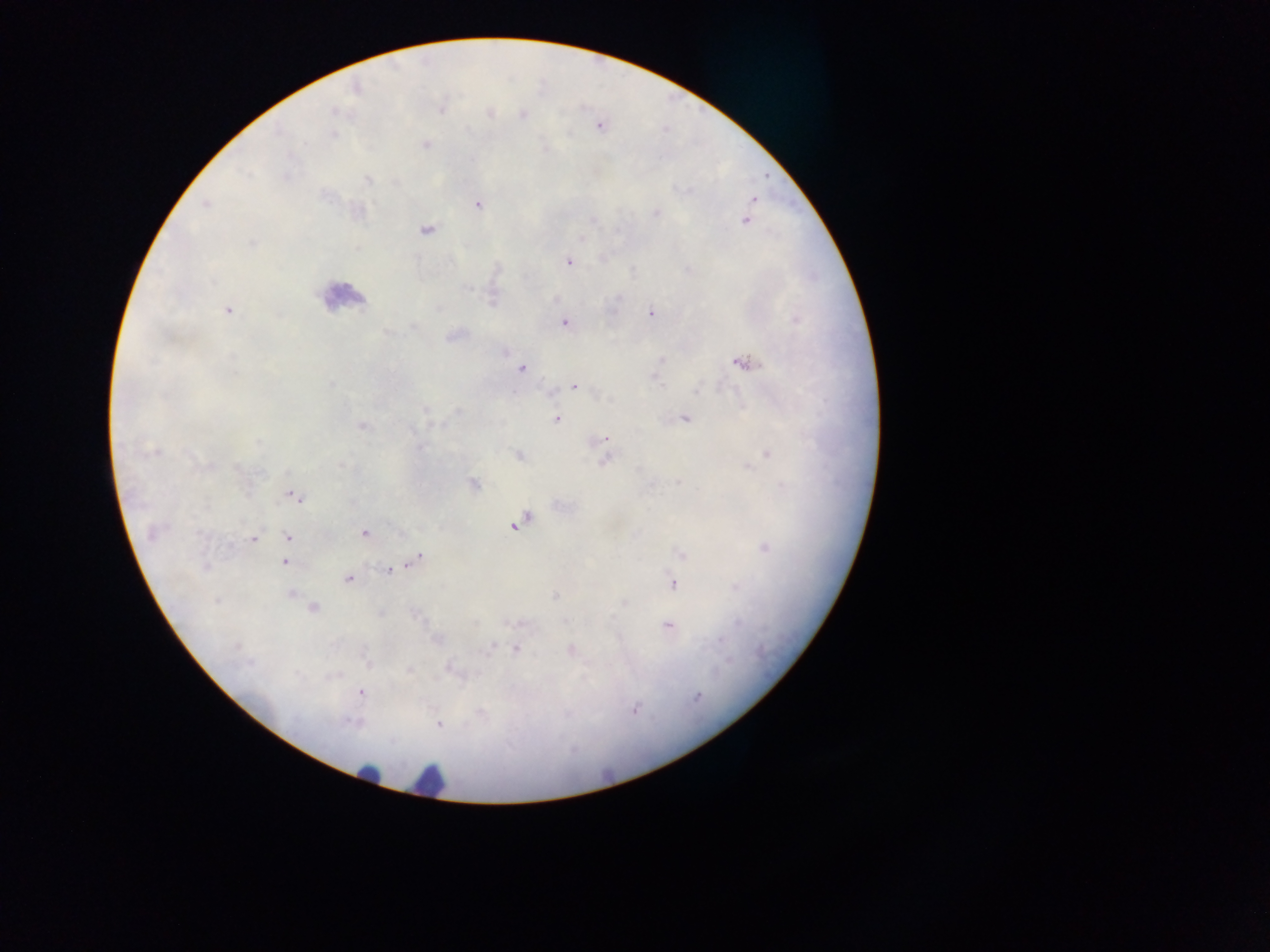 Approximate centers as (x, y) in pixels. Plasmodium parasite locations: (441, 106), (487, 114), (523, 115), (599, 126), (426, 144), (368, 179), (753, 200), (478, 203), (356, 211), (655, 212), (745, 220), (425, 229), (567, 262), (227, 310), (651, 313), (565, 321), (454, 334), (661, 361), (743, 363), (521, 368), (575, 385), (685, 417), (556, 418), (361, 425), (606, 438), (519, 455), (766, 455), (604, 459), (472, 484), (293, 495), (518, 522), (153, 532), (363, 533), (289, 536), (253, 538), (764, 548), (681, 553), (415, 559), (285, 562), (206, 566), (390, 569), (348, 579), (672, 583), (290, 593), (313, 608), (667, 626), (492, 647), (517, 648), (570, 649), (450, 667), (407, 670), (360, 692), (633, 709), (438, 725). Leukocyte locations: (340, 296), (368, 775), (429, 781). Image is 1270×952 pixels. Photographed through a microscope with a mobile-phone camera. Collected in Ghana. Single field of view. Thick blood film.